Point out each Plasmodium parasite.
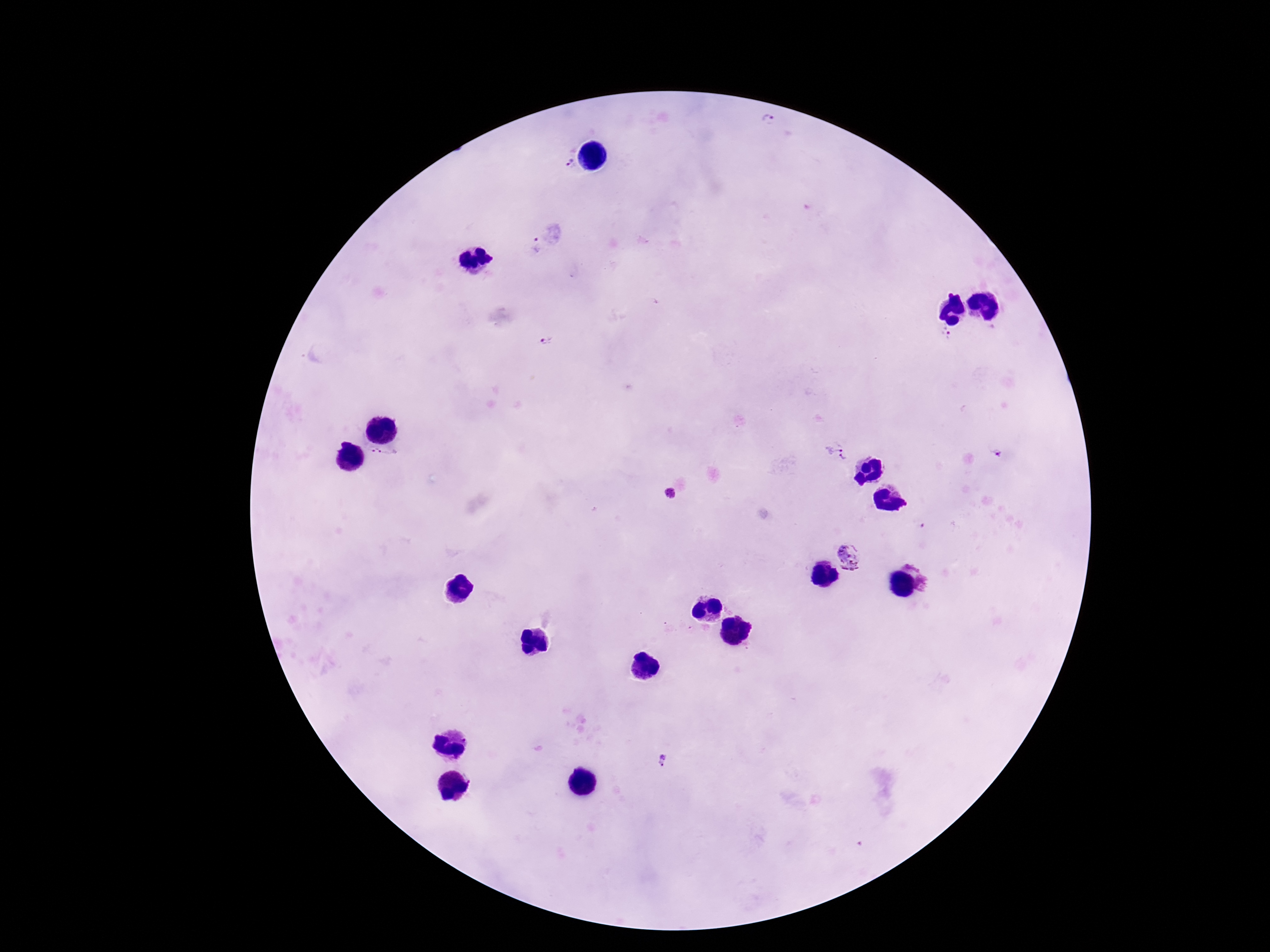
Approximate centers as {x, y} in pixels.
Plasmodium parasites: {767, 119}, {566, 165}, {535, 244}, {946, 333}, {545, 342}, {831, 444}, {997, 454}, {843, 458}, {669, 494}, {919, 524}, {850, 557}, {663, 760}.

Summary:
  - Patient malaria status: infected
  - Stain: Giemsa
  - Magnification: 100x
  - Capture: smartphone camera through the microscope eyepiece
  - Preparation: thick peripheral-blood smear
  - Field of view: one from this slide
  - Image size: 1270×952 pixels